Assess the morphology of the red blood cells.
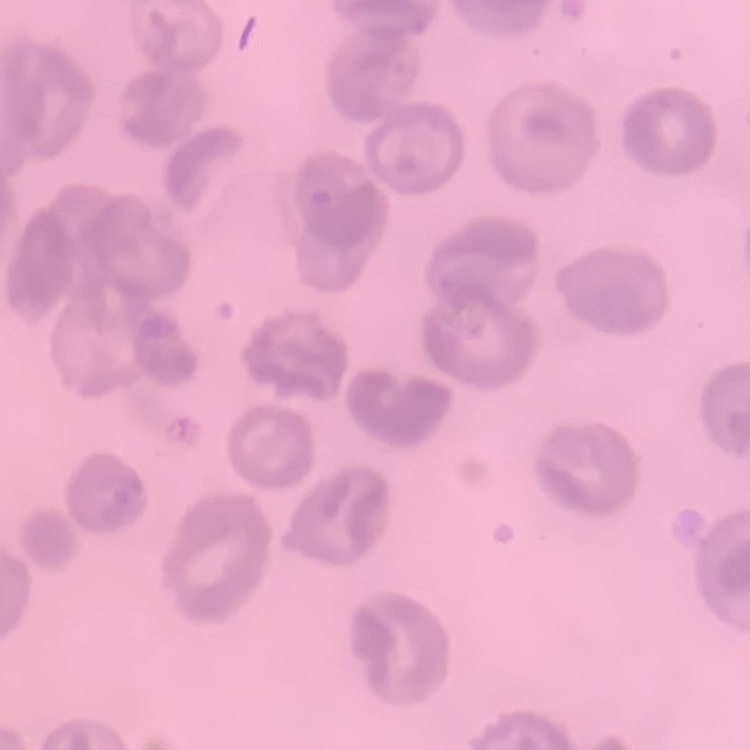
No rouleaux formation.

Thin peripheral smear. One tile cut from a larger photomicrograph. Stained with either Field's or Giemsa.